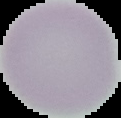

Image is 121×118 pixels. Malaria status: uninfected. From a thin blood film. Segmented cell region on a black background.